Comment on the morphology of the red blood cells.
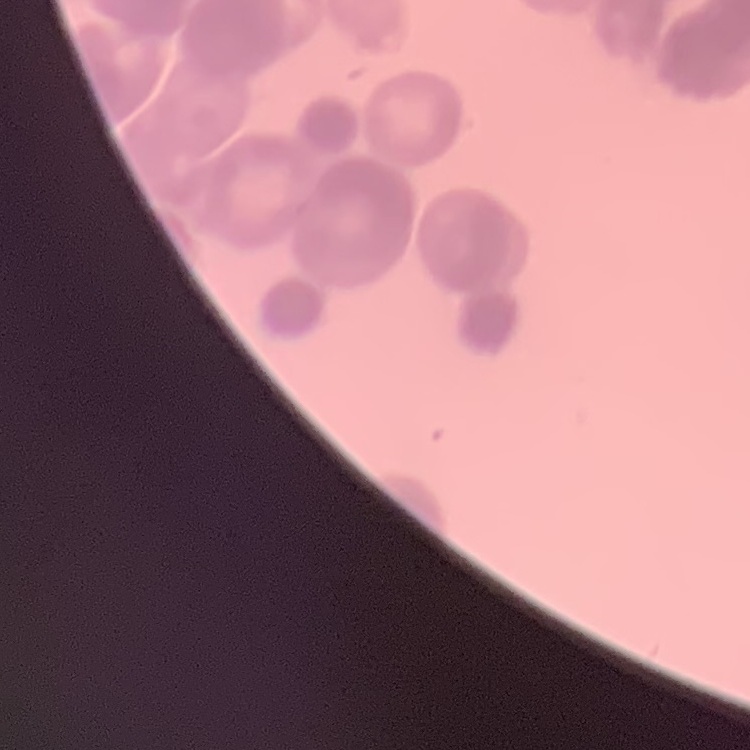
Rouleaux formation.

{
  "stain": "Field's or Giemsa",
  "preparation": "thin peripheral smear",
  "image_type": "one tile cut from a larger photomicrograph"
}